Locate every Plasmodium malariae-infected red blood cell.
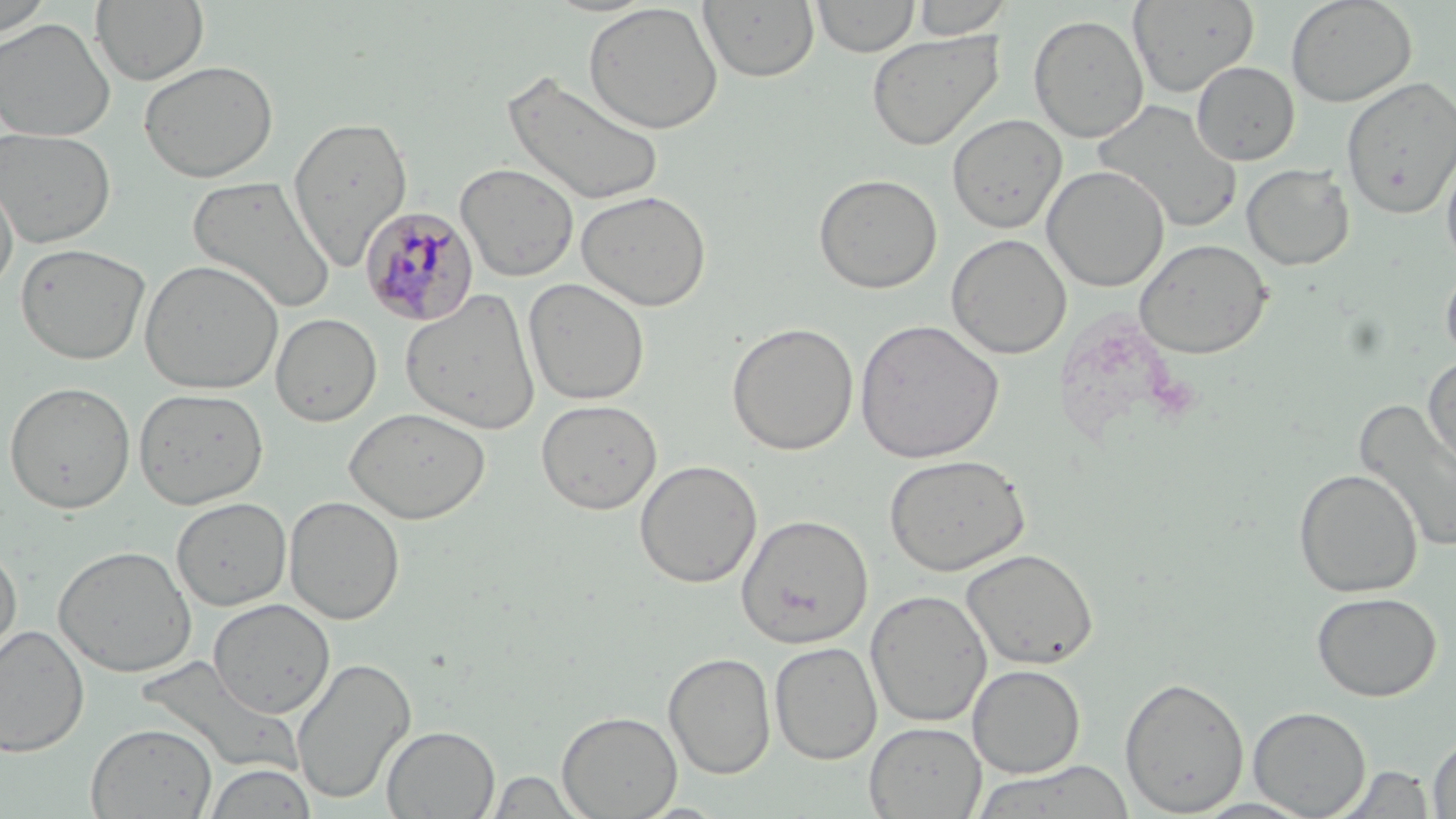
Approximate bounding boxes as [x1, y1, x2, y2] in pixels.
Plasmodium malariae-infected red blood cells: [360, 205, 479, 327].

Uninfected red blood cell locations: [0, 0, 55, 39], [698, 0, 819, 83], [810, 0, 919, 58], [910, 0, 1013, 39], [1128, 0, 1259, 97], [1285, 0, 1417, 107], [91, 1, 210, 86], [583, 2, 723, 135], [1028, 14, 1149, 143], [0, 17, 116, 142], [866, 30, 1005, 150], [138, 60, 278, 182], [1191, 61, 1299, 165], [500, 70, 665, 207], [1341, 76, 1455, 219], [1093, 99, 1243, 233], [946, 114, 1067, 233], [288, 115, 413, 270], [0, 128, 116, 247], [1439, 141, 1456, 272], [455, 162, 579, 282], [1241, 163, 1354, 271], [1042, 165, 1169, 292], [0, 170, 18, 296], [813, 173, 943, 294], [187, 175, 337, 314], [576, 189, 712, 311], [946, 233, 1071, 359], [1134, 238, 1273, 359], [15, 242, 151, 365], [139, 258, 284, 395], [1440, 259, 1456, 367], [522, 278, 650, 405], [401, 288, 541, 434], [271, 312, 382, 427], [853, 318, 1005, 464], [726, 321, 859, 456], [1422, 352, 1456, 478], [3, 381, 136, 514], [133, 387, 269, 509], [1354, 398, 1456, 554], [536, 399, 662, 515], [344, 407, 491, 524], [883, 453, 1031, 576], [634, 459, 763, 588], [1293, 468, 1423, 598], [284, 495, 405, 625], [171, 497, 292, 611], [735, 513, 873, 649], [0, 544, 22, 671], [53, 544, 198, 678], [960, 547, 1098, 670], [865, 589, 993, 727], [1311, 591, 1442, 702], [208, 598, 335, 718], [0, 625, 89, 756], [769, 641, 883, 764], [664, 652, 776, 779], [291, 657, 415, 805], [967, 664, 1085, 778], [1119, 675, 1249, 816], [1248, 706, 1371, 817], [557, 710, 682, 818], [85, 722, 217, 818], [864, 722, 986, 818], [382, 725, 500, 818], [1427, 732, 1456, 818], [972, 760, 1137, 818], [203, 763, 318, 819], [1334, 765, 1437, 818], [486, 770, 588, 817]. Slide-level diagnosis: Plasmodium malariae. 1000x magnification. One field of a larger specimen. Thin blood smear. Light microscopy. May-Grünwald-Giemsa stain. Image is 1456×819 pixels.